Classify this cell by malaria status.
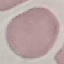

Uninfected.

image_type: automatically extracted cell patch, resized to 64 × 64 pixels
stain: Giemsa
capture: smartphone through the microscope eyepiece
preparation: thin blood film